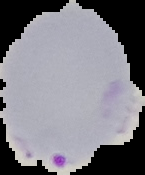
Summary:
  - Image size: 145×175 pixels
  - Malaria status: parasitized
  - Image type: segmented cell region with the area outside set to black
  - Preparation: thin blood film